Identify the blood parasite species.
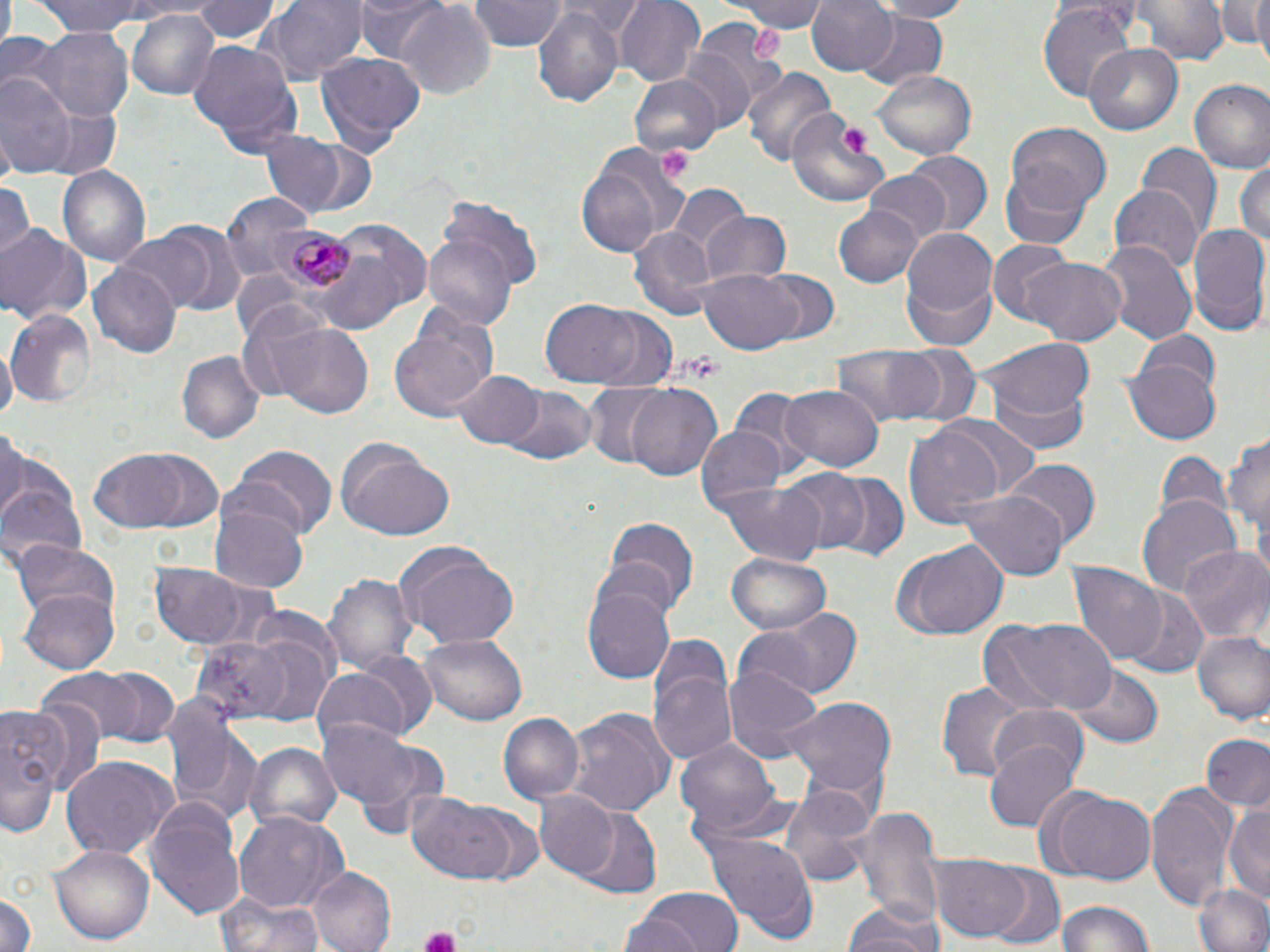

Plasmodium malariae.

uninfected_red_blood_cell_locations: 'approximate bounding boxes as (x1,y1)-(x2,y2) corner pairs in pixels: (26,0)-(176,36), (193,0)-(277,44), (268,0)-(370,82), (357,0)-(447,63), (467,0)-(567,52), (564,0)-(640,39), (614,0)-(706,85), (738,0)-(829,31), (804,0)-(897,75), (868,0)-(968,21), (1134,0)-(1226,64), (1222,0)-(1268,57), (1248,0)-(1270,69), (394,3)-(497,98), (1038,4)-(1137,102), (532,6)-(625,108), (130,8)-(218,101), (854,10)-(948,91), (689,16)-(789,115), (26,31)-(132,121), (186,41)-(302,154), (1084,43)-(1183,135), (679,47)-(755,129), (315,51)-(426,151), (741,65)-(833,166), (872,71)-(977,160), (1,74)-(75,177), (627,75)-(721,160), (1187,78)-(1270,174), (787,109)-(889,208), (1007,124)-(1110,215), (256,132)-(363,217), (1137,144)-(1222,236), (578,145)-(684,258), (902,153)-(991,236), (1234,160)-(1270,254), (57,167)-(150,267), (863,170)-(953,242), (998,172)-(1092,248), (0,181)-(31,265), (1109,184)-(1202,275), (670,185)-(749,269), (220,193)-(314,278), (437,196)-(544,293), (835,205)-(922,287), (698,209)-(791,284), (321,220)-(431,316), (1185,223)-(1270,335), (0,224)-(90,327), (628,227)-(715,320), (901,227)-(996,323), (114,229)-(221,311), (423,233)-(519,331), (987,239)-(1077,326), (1097,240)-(1196,345), (312,251)-(407,331), (1025,256)-(1126,343), (89,262)-(179,358), (698,266)-(803,353), (758,271)-(841,346), (900,272)-(1000,351), (540,298)-(648,387), (7,311)-(96,408), (390,319)-(496,423), (273,322)-(373,419), (1136,330)-(1222,398), (982,337)-(1095,423), (1,339)-(16,424), (829,344)-(962,428), (901,345)-(982,428), (178,353)-(262,443), (1124,357)-(1221,444), (453,369)-(541,450), (984,381)-(1091,456), (580,383)-(672,466), (781,383)-(883,470), (627,384)-(722,482), (729,385)-(815,472), (502,386)-(597,466), (942,417)-(1042,500), (903,421)-(1010,527), (1225,424)-(1270,548), (695,426)-(786,514), (0,427)-(25,520), (337,439)-(455,540), (231,445)-(338,540), (1151,445)-(1229,524), (88,447)-(220,532), (1007,459)-(1099,548), (0,465)-(85,571), (777,469)-(873,556), (824,473)-(909,563), (714,482)-(829,563), (957,487)-(1071,580), (1139,497)-(1241,599), (210,502)-(309,593), (599,515)-(700,618), (9,540)-(120,624), (393,540)-(519,649), (892,543)-(1008,641), (1179,547)-(1269,644), (724,554)-(830,638), (151,560)-(263,650), (1068,563)-(1168,668), (326,570)-(416,676), (583,583)-(676,684), (20,588)-(120,674), (1120,589)-(1211,680), (748,605)-(865,701), (978,616)-(1117,717), (1191,630)-(1270,727), (196,631)-(331,726), (420,634)-(528,725), (645,647)-(739,771), (345,650)-(436,738), (725,665)-(823,766), (42,666)-(178,748), (1069,666)-(1162,749), (309,669)-(411,748), (935,677)-(1024,782), (163,693)-(255,819), (786,697)-(896,802), (0,699)-(75,834), (987,704)-(1090,784), (565,709)-(674,815), (500,713)-(584,802), (321,720)-(422,810), (1199,732)-(1270,813), (675,739)-(780,836), (351,740)-(453,840), (985,740)-(1079,831), (246,742)-(339,833), (61,757)-(174,862), (1145,782)-(1236,906), (779,784)-(882,890), (1050,790)-(1158,886), (533,791)-(621,882), (405,792)-(514,883), (147,795)-(245,919), (1223,805)-(1270,904), (463,806)-(544,885), (850,806)-(942,925), (566,807)-(662,899), (236,811)-(346,914), (708,832)-(819,942), (48,843)-(155,945), (931,854)-(1031,941), (311,866)-(397,952), (985,870)-(1065,950), (1193,881)-(1270,952), (632,886)-(746,952), (0,888)-(37,952), (216,891)-(324,952), (1056,899)-(1156,952), (841,902)-(947,952)'
plasmodium_malariae_infected_red_blood_cell_locations: 'approximate bounding boxes as (x1,y1)-(x2,y2) corner pairs in pixels: (273,227)-(357,298)'
platelet_locations: 'approximate bounding boxes as (x1,y1)-(x2,y2) corner pairs in pixels: (747,24)-(783,66), (840,127)-(869,156), (655,144)-(693,181), (418,925)-(462,952)'
image_size: 1270×952 pixels
stain: May-Grünwald-Giemsa
preparation: thin blood film
modality: light microscopy
field_of_view: single
magnification: 1000x